Describe the morphology of the erythrocytes.
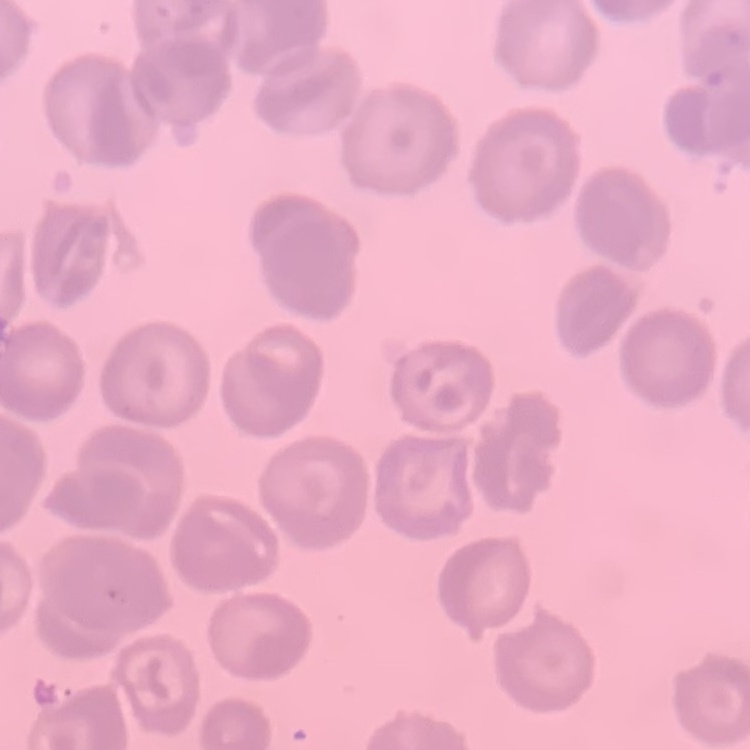
They show no rouleaux formation.

stain: Field's or Giemsa
image_type: one tile cut from a larger photomicrograph
preparation: thin peripheral smear